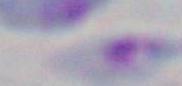

Summary:
  - Modality: photomicrograph
  - Identification: Toxoplasma gondii
  - Magnification: 1000x